Classify this cell by malaria status.
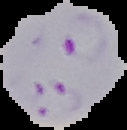
It is parasitized.

The area outside the segmented cell region is set to black. Image is 127×130 pixels. From a thin blood film.